Outline platelets.
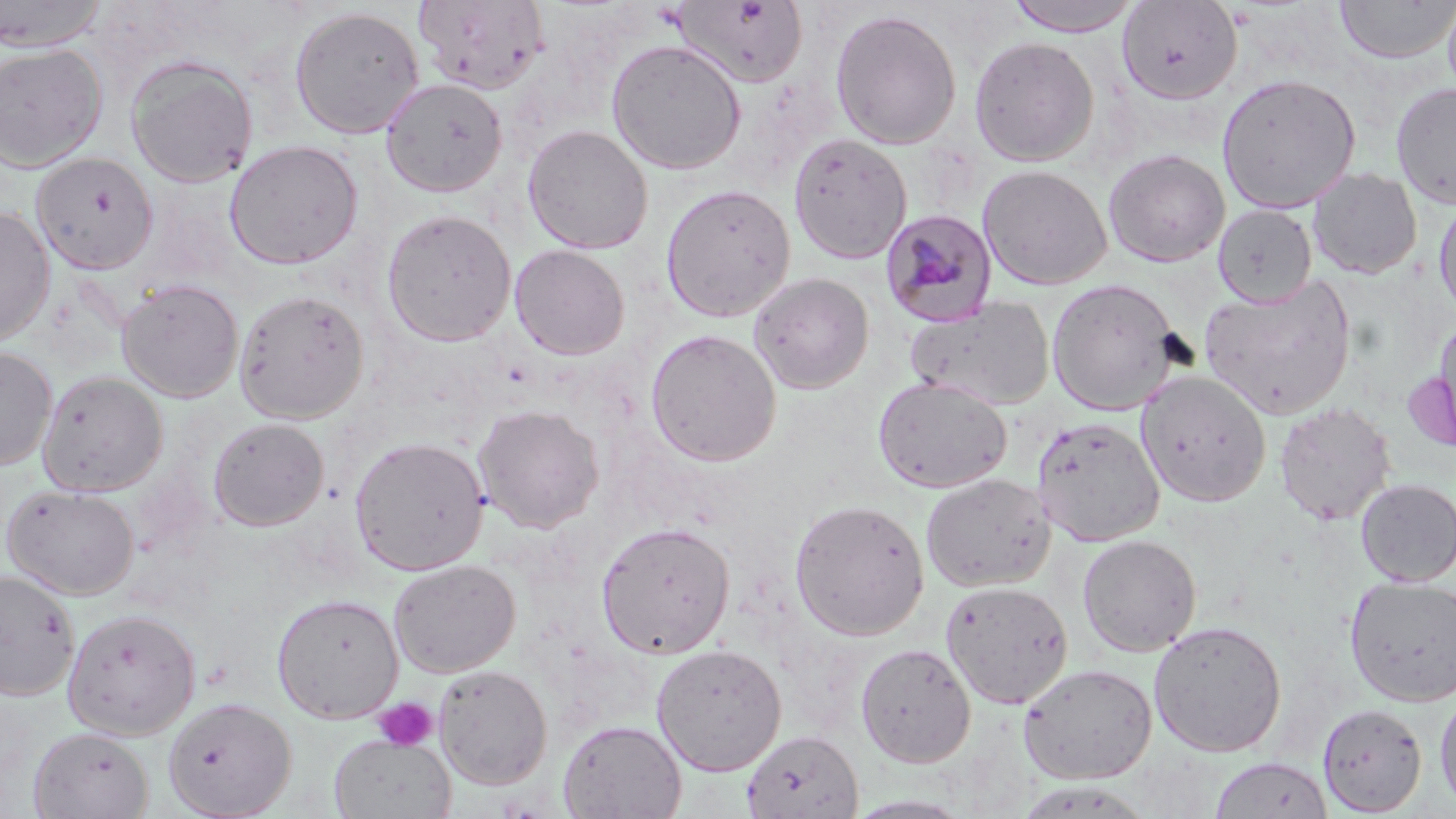
Approximate bounding boxes as named x1/y1/x2/y2 corners in pixels.
Platelets: (x1=371, y1=697, x2=439, y2=751).

Plasmodium malariae-infected red blood cell locations: (x1=880, y1=208, x2=999, y2=328). Uninfected red blood cell locations: (x1=0, y1=0, x2=108, y2=51), (x1=414, y1=0, x2=548, y2=95), (x1=1001, y1=0, x2=1146, y2=36), (x1=1333, y1=0, x2=1456, y2=65), (x1=1441, y1=0, x2=1456, y2=104), (x1=671, y1=1, x2=810, y2=88), (x1=1116, y1=2, x2=1243, y2=104), (x1=289, y1=6, x2=424, y2=140), (x1=829, y1=8, x2=962, y2=150), (x1=968, y1=35, x2=1100, y2=167), (x1=605, y1=38, x2=747, y2=175), (x1=0, y1=43, x2=108, y2=172), (x1=125, y1=55, x2=258, y2=188), (x1=1216, y1=72, x2=1361, y2=214), (x1=380, y1=77, x2=508, y2=197), (x1=1390, y1=81, x2=1456, y2=211), (x1=522, y1=124, x2=653, y2=255), (x1=788, y1=132, x2=912, y2=264), (x1=223, y1=139, x2=364, y2=270), (x1=1103, y1=148, x2=1230, y2=268), (x1=31, y1=152, x2=159, y2=274), (x1=978, y1=164, x2=1112, y2=290), (x1=1307, y1=167, x2=1423, y2=280), (x1=660, y1=184, x2=796, y2=322), (x1=1433, y1=196, x2=1456, y2=321), (x1=1213, y1=203, x2=1317, y2=307), (x1=0, y1=207, x2=56, y2=347), (x1=381, y1=209, x2=516, y2=347), (x1=509, y1=244, x2=630, y2=360), (x1=749, y1=272, x2=875, y2=394), (x1=1199, y1=274, x2=1357, y2=420), (x1=1046, y1=278, x2=1183, y2=416), (x1=116, y1=279, x2=244, y2=402), (x1=234, y1=289, x2=370, y2=424), (x1=904, y1=296, x2=1056, y2=411), (x1=1433, y1=311, x2=1456, y2=445), (x1=644, y1=328, x2=782, y2=466), (x1=0, y1=346, x2=57, y2=470), (x1=37, y1=371, x2=168, y2=497), (x1=1136, y1=371, x2=1272, y2=507), (x1=873, y1=376, x2=1012, y2=492), (x1=1274, y1=401, x2=1396, y2=526), (x1=472, y1=404, x2=605, y2=533), (x1=1031, y1=415, x2=1165, y2=546), (x1=207, y1=417, x2=329, y2=531), (x1=349, y1=435, x2=490, y2=575), (x1=920, y1=473, x2=1056, y2=593), (x1=1355, y1=478, x2=1456, y2=587), (x1=2, y1=484, x2=140, y2=599), (x1=789, y1=499, x2=930, y2=641), (x1=596, y1=521, x2=735, y2=659), (x1=1077, y1=534, x2=1202, y2=656), (x1=388, y1=559, x2=522, y2=678), (x1=0, y1=569, x2=79, y2=701), (x1=1344, y1=576, x2=1456, y2=708), (x1=940, y1=580, x2=1073, y2=709), (x1=271, y1=593, x2=403, y2=723), (x1=61, y1=606, x2=201, y2=740), (x1=1148, y1=620, x2=1287, y2=757), (x1=855, y1=642, x2=976, y2=767), (x1=650, y1=643, x2=787, y2=776), (x1=1017, y1=662, x2=1157, y2=784), (x1=433, y1=665, x2=552, y2=790), (x1=1434, y1=686, x2=1456, y2=813), (x1=162, y1=696, x2=296, y2=818), (x1=1317, y1=703, x2=1427, y2=816), (x1=558, y1=719, x2=687, y2=818), (x1=28, y1=726, x2=154, y2=819), (x1=741, y1=729, x2=863, y2=819), (x1=329, y1=733, x2=455, y2=818), (x1=1208, y1=754, x2=1334, y2=819), (x1=841, y1=794, x2=978, y2=818). Slide-level diagnosis: Plasmodium malariae. One field of a larger specimen. Image is 1456×819 pixels. Thin blood film. May-Grünwald-Giemsa-stained preparation. Light microscopy. 1000x magnification.